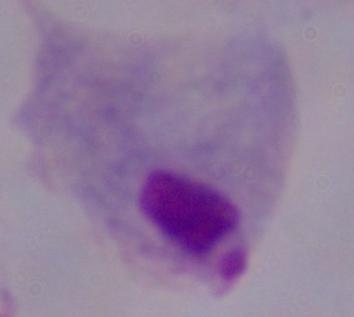
Captured at 1000x magnification. A trichomonad is seen. Photomicrograph.